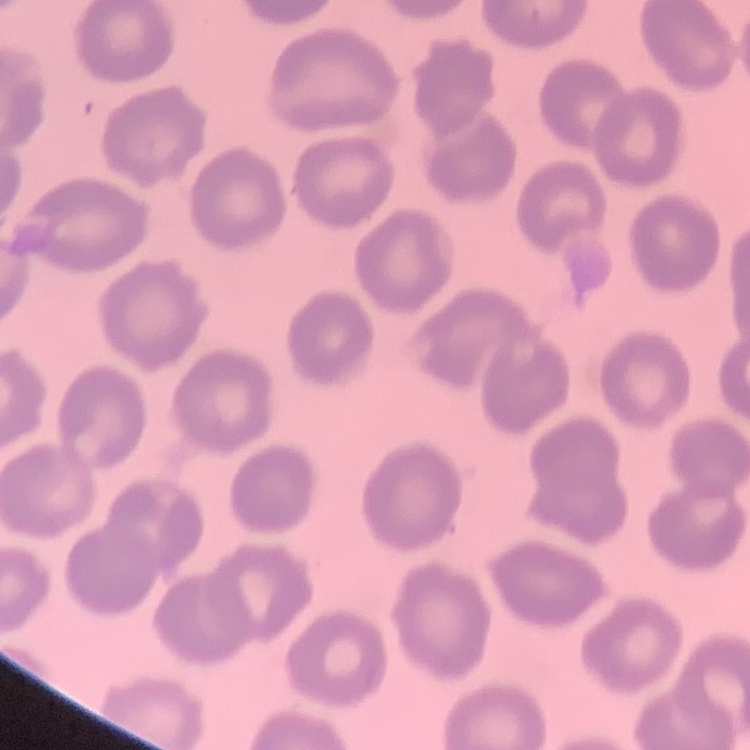 The erythrocytes show no rouleaux formation. Thin blood smear. Field's or Giemsa stain. One tile cut from a larger photomicrograph.